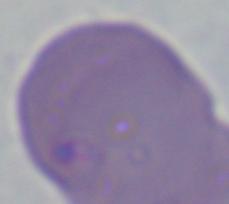

Summary:
  - Modality: photomicrograph
  - Magnification: 1000x
  - Identification: Babesia